Give the position of every Plasmodium parasite.
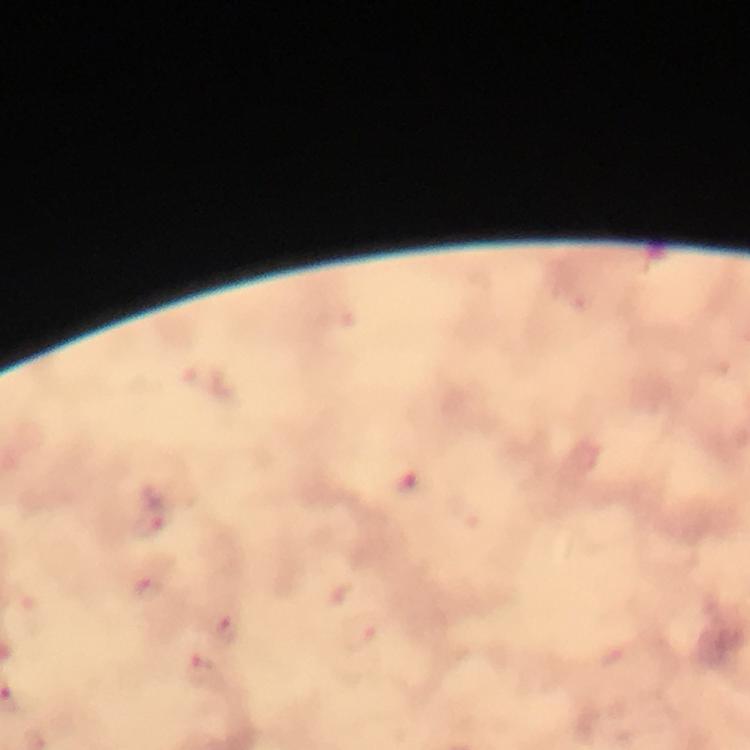
Approximate centers as [x, y] in pixels.
Plasmodium parasites: [415, 483], [150, 519], [150, 588], [224, 630].

Thick blood film. Image is 750×750 pixels. Cropped region of a single field of view. Giemsa stain. From a malaria diagnostic workup. Immersion oil was used. 100x magnification. Photographed with a smartphone mounted on the microscope.